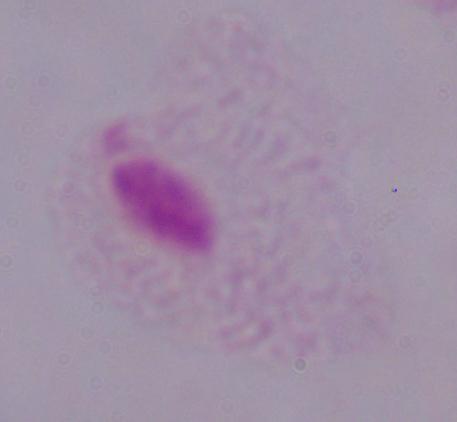
A trichomonad is seen. Captured at 1000x magnification. Photomicrograph.